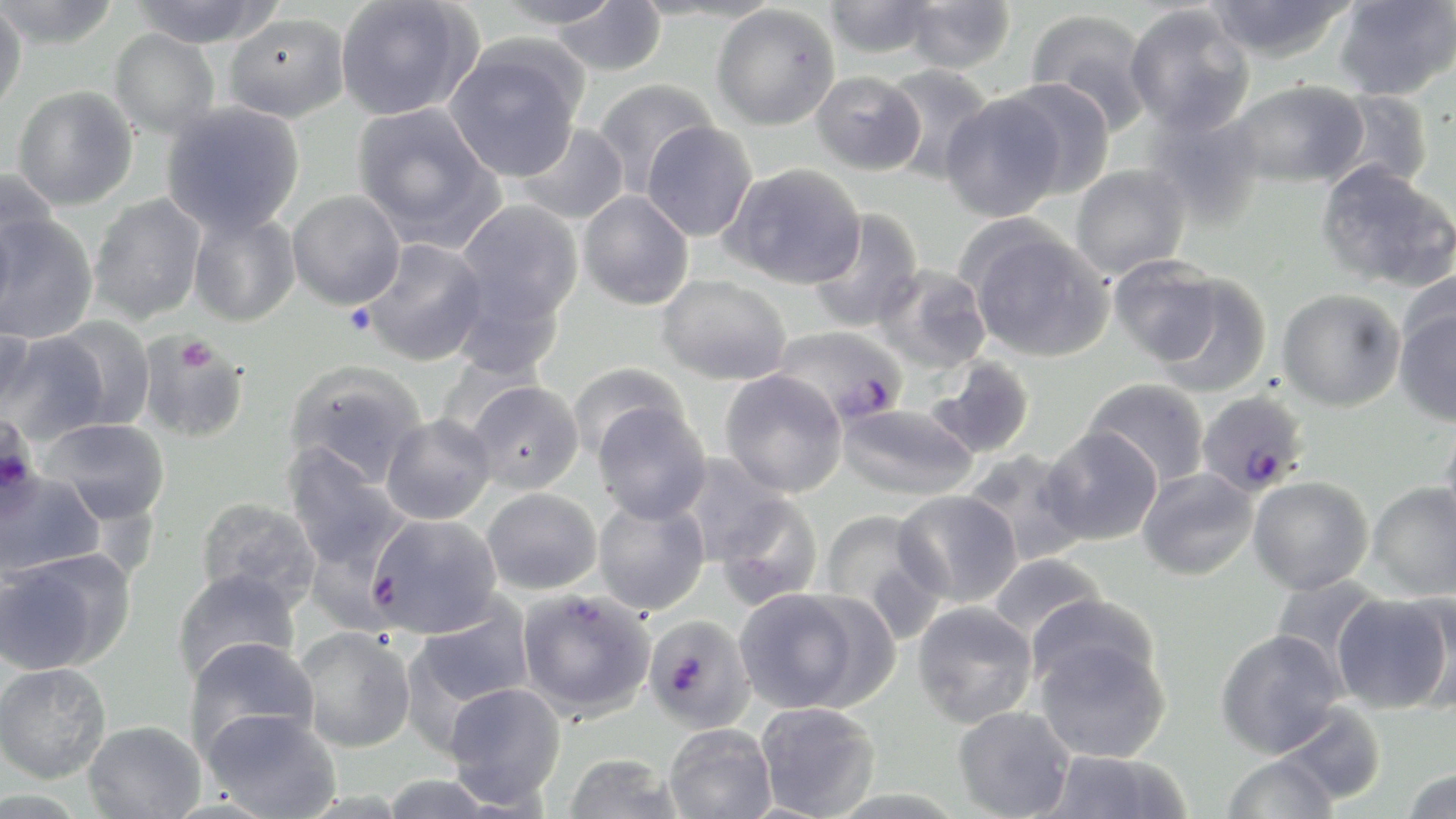
Plasmodium falciparum-infected red blood cell locations = approximate bounding boxes as (x1,y1)-(x2,y2) corner pairs in pixels: (771,326)-(909,428), (1196,390)-(1311,498), (1,411)-(46,528), (365,513)-(502,639), (517,588)-(656,722), (643,614)-(755,732)
slide-level diagnosis = Plasmodium falciparum
uninfected red blood cell locations = approximate bounding boxes as (x1,y1)-(x2,y2) corner pairs in pixels: (0,0)-(122,50), (129,0)-(283,49), (334,0)-(480,121), (492,0)-(625,29), (903,0)-(1014,73), (1205,0)-(1353,63), (1331,0)-(1456,101), (548,1)-(667,76), (823,1)-(939,58), (0,2)-(27,116), (1124,3)-(1256,136), (711,4)-(840,131), (1026,8)-(1156,132), (224,13)-(349,122), (109,29)-(220,139), (444,41)-(584,182), (881,63)-(996,183), (811,71)-(925,174), (593,78)-(717,196), (1001,79)-(1115,199), (1231,79)-(1368,188), (12,85)-(138,210), (1324,89)-(1434,192), (940,92)-(1065,222), (160,101)-(305,236), (351,102)-(502,248), (1141,108)-(1269,229), (641,120)-(757,242), (514,121)-(629,225), (1315,161)-(1455,293), (723,163)-(866,289), (1070,164)-(1191,279), (0,166)-(57,287), (287,190)-(405,309), (578,191)-(694,310), (88,194)-(207,325), (457,200)-(583,325), (806,209)-(924,333), (188,210)-(301,327), (0,213)-(99,343), (966,225)-(1114,363), (359,239)-(489,366), (1108,256)-(1220,365), (872,264)-(992,375), (1152,273)-(1272,397), (656,274)-(793,384), (1277,288)-(1406,412), (1394,303)-(1456,426), (0,315)-(36,418), (50,315)-(156,431), (0,331)-(110,445), (136,331)-(251,444), (928,356)-(1036,459), (285,360)-(428,488), (569,362)-(687,459), (719,369)-(848,497), (1083,377)-(1209,488), (465,380)-(584,494), (836,401)-(978,500), (591,402)-(711,523), (381,413)-(496,525), (41,417)-(171,525), (1439,417)-(1456,538), (1041,426)-(1162,546), (283,445)-(410,572), (962,450)-(1089,566), (678,454)-(798,570), (1137,467)-(1258,581), (0,471)-(105,582), (1248,476)-(1374,594), (1367,481)-(1456,600), (482,487)-(602,594), (894,490)-(1022,608), (709,491)-(824,610), (193,496)-(322,611), (593,497)-(710,616), (817,508)-(945,637), (0,550)-(132,675), (987,552)-(1106,643), (172,568)-(301,685), (1269,573)-(1388,682), (733,587)-(871,713), (1332,592)-(1453,714), (1027,593)-(1161,697), (406,599)-(535,729), (912,601)-(1038,728), (294,627)-(416,752), (1214,628)-(1346,758), (1034,635)-(1171,763), (184,636)-(319,759), (0,662)-(111,784), (443,681)-(566,807), (755,702)-(881,818), (1274,702)-(1387,806), (952,706)-(1074,819), (202,709)-(342,818), (83,719)-(206,819), (663,723)-(777,818), (1039,751)-(1190,818), (563,752)-(684,819), (1221,753)-(1338,818), (1401,768)-(1456,818), (376,774)-(502,818)
modality = light microscopy
preparation = thin blood smear
platelet locations = approximate bounding boxes as (x1,y1)-(x2,y2) corner pairs in pixels: (344,303)-(376,337), (178,336)-(215,374)
field of view = one of a larger specimen
image size = 1456×819 pixels
stain = May-Grünwald-Giemsa
magnification = 1000x